Locate every malaria parasite.
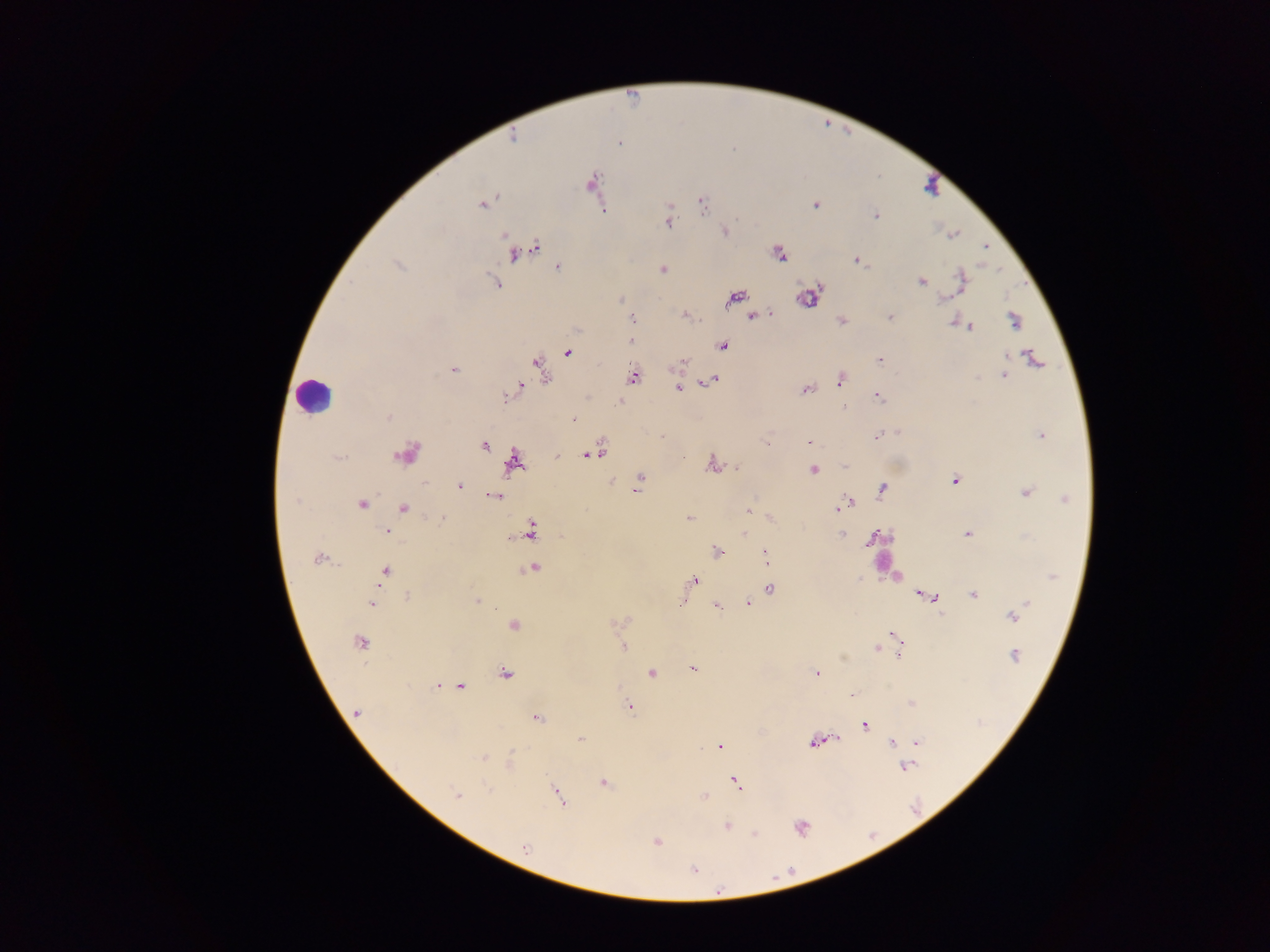
Approximate centers as (x, y) in pixels.
Malaria parasites: (618, 143), (591, 183), (702, 203), (483, 204), (815, 205), (875, 215), (668, 222), (725, 231), (954, 234), (986, 247), (535, 248), (529, 250), (515, 253), (779, 254), (858, 260), (558, 268), (663, 269), (961, 281), (921, 282), (496, 284), (735, 297), (809, 298), (941, 299), (752, 317), (890, 318), (632, 319), (842, 320), (1014, 320), (954, 321), (970, 327), (631, 341), (722, 347), (568, 353), (880, 360), (1035, 360), (682, 362), (541, 367), (454, 370), (1004, 375), (634, 377), (841, 380), (710, 381), (679, 388), (806, 389), (515, 390), (878, 397), (388, 418), (573, 419), (1041, 435), (662, 436), (875, 437), (809, 443), (767, 444), (484, 446), (594, 453), (407, 454), (558, 455), (586, 455), (514, 463), (712, 464), (844, 466), (737, 467), (813, 469), (639, 480), (955, 480), (424, 482), (459, 486), (637, 487), (882, 490), (1027, 492), (493, 496), (1065, 499), (296, 501), (362, 504), (847, 504), (403, 508), (838, 508), (750, 510), (689, 518), (772, 518), (442, 519), (386, 531), (531, 532), (744, 532), (968, 534), (842, 535), (870, 541), (718, 552), (765, 555), (318, 558), (534, 569), (384, 572), (1052, 576), (858, 579), (695, 580), (769, 589), (922, 594), (974, 594), (406, 596), (934, 598), (477, 601), (748, 603), (372, 604), (1025, 604), (716, 605), (1014, 616), (513, 624), (895, 635), (359, 643), (624, 648), (877, 649), (899, 651), (1014, 655), (693, 668), (652, 673), (505, 674), (817, 674), (438, 686), (460, 686), (852, 696), (911, 703), (630, 706), (357, 713), (537, 717), (865, 724), (837, 738), (580, 739), (813, 742), (892, 742), (918, 742), (719, 746), (483, 758), (509, 762), (906, 766), (736, 782), (604, 783), (488, 788), (457, 795), (558, 796), (704, 796), (727, 826), (801, 827), (755, 834), (656, 842), (524, 847), (694, 870), (718, 891).

Leukocyte locations: (314, 396). Collected in Ghana. Mobile-phone photograph taken through the microscope. Single field of view. Thick blood smear. Image is 1270×952 pixels.